Describe the morphology of the erythrocytes.
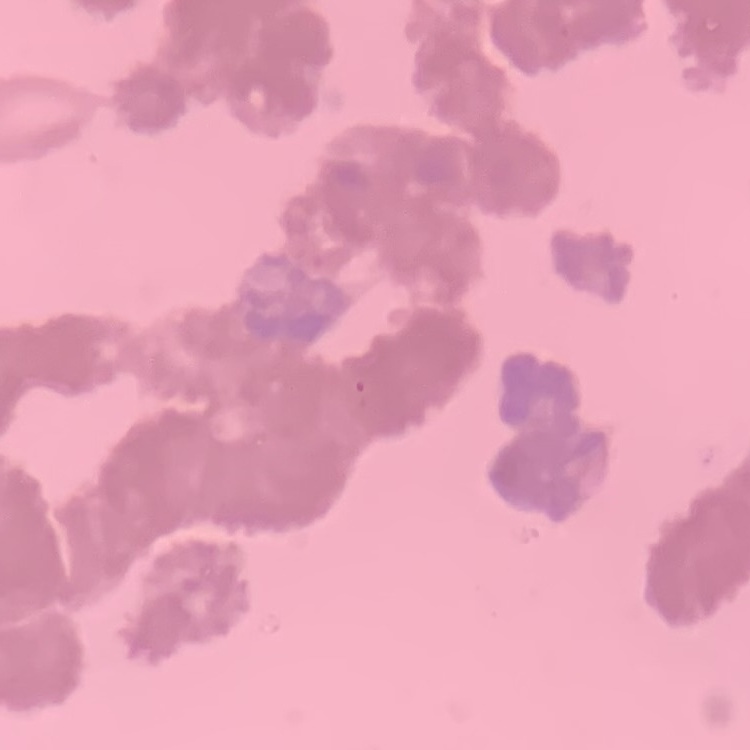
Rouleaux formation.

Summary:
  - Image type: square crop of a larger photomicrograph
  - Stain: Field's or Giemsa
  - Preparation: thin blood film